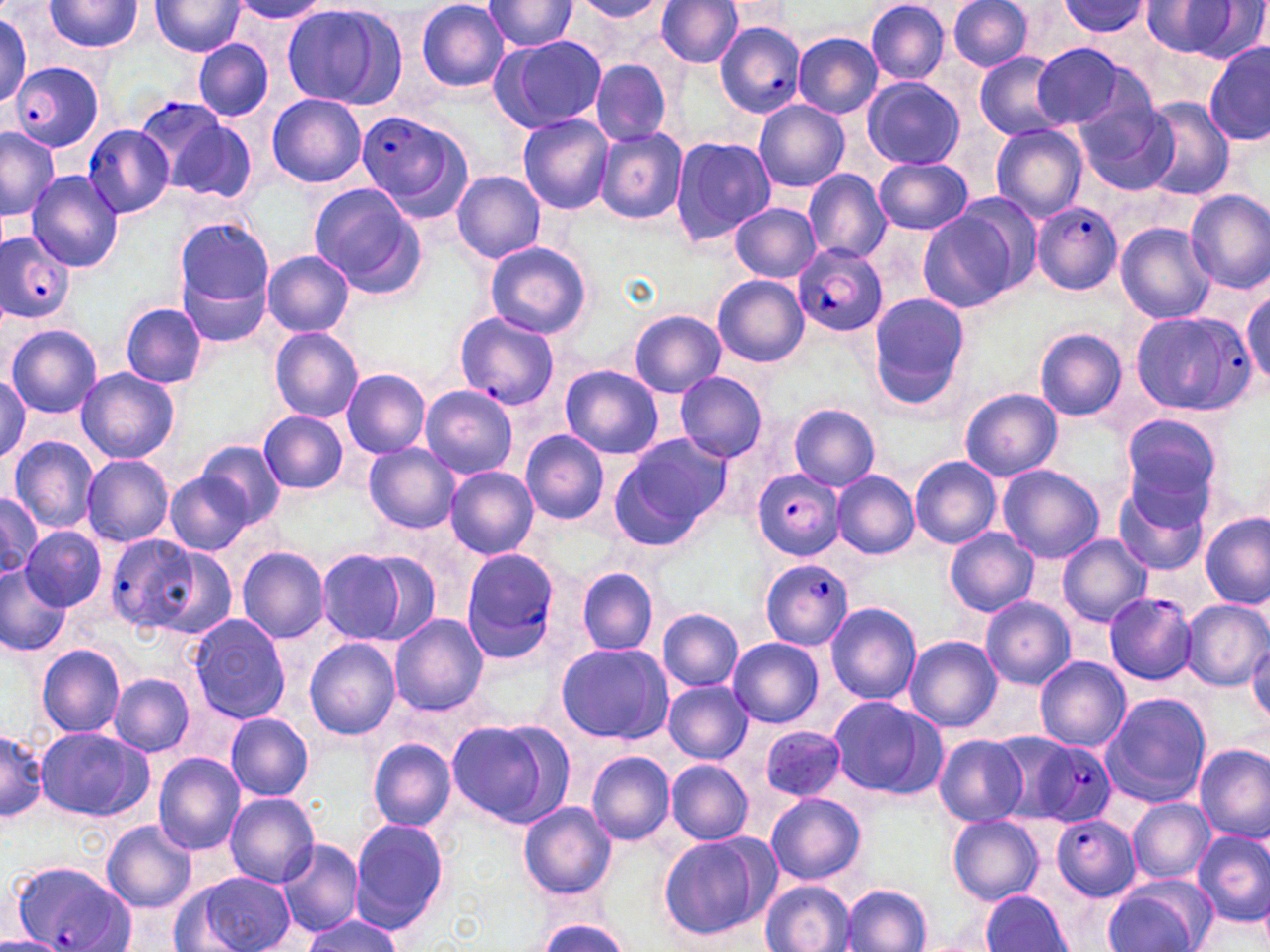
Summary:
  - Coordinate format: approximate bounding boxes as (x1, y1, x2, y2) in pixels
  - Plasmodium falciparum-infected red blood cell locations: (714, 21, 808, 118), (11, 62, 103, 150), (130, 94, 227, 188), (356, 110, 471, 217), (84, 124, 174, 218), (1032, 202, 1123, 295), (2, 232, 75, 322), (793, 244, 888, 337), (1130, 308, 1259, 419), (454, 312, 560, 412), (753, 471, 846, 558), (106, 534, 200, 632), (458, 547, 566, 662), (760, 559, 854, 650), (1104, 592, 1198, 684), (1016, 733, 1118, 829), (1051, 816, 1141, 899), (11, 860, 132, 952)
  - Uninfected red blood cell locations: (45, 0, 144, 52), (484, 0, 578, 53), (719, 0, 794, 29), (865, 0, 949, 83), (946, 0, 1036, 72), (150, 1, 246, 57), (232, 1, 329, 25), (416, 1, 509, 91), (571, 1, 667, 22), (1052, 1, 1155, 40), (658, 2, 745, 69), (280, 3, 401, 110), (1138, 3, 1255, 60), (0, 11, 32, 109), (791, 31, 882, 118), (490, 34, 607, 132), (193, 39, 274, 121), (1030, 42, 1130, 128), (1204, 43, 1268, 144), (974, 51, 1073, 140), (591, 60, 673, 146), (861, 77, 964, 169), (267, 92, 368, 188), (1072, 96, 1179, 197), (1141, 98, 1235, 201), (754, 100, 849, 193), (518, 113, 613, 214), (171, 118, 258, 206), (990, 124, 1086, 223), (594, 128, 688, 225), (0, 129, 59, 220), (670, 133, 776, 246), (871, 157, 973, 234), (26, 171, 123, 273), (452, 171, 546, 262), (802, 171, 890, 262), (309, 184, 424, 297), (1185, 191, 1269, 293), (949, 194, 1042, 295), (728, 203, 822, 282), (917, 209, 1019, 310), (175, 218, 275, 307), (1116, 222, 1218, 325), (166, 227, 330, 331), (484, 242, 593, 340), (261, 251, 355, 337), (177, 263, 274, 348), (713, 275, 810, 367), (1241, 284, 1270, 388), (866, 294, 971, 409), (119, 302, 208, 389), (628, 310, 726, 397), (6, 324, 102, 417), (269, 326, 363, 423), (1034, 327, 1128, 422), (559, 365, 663, 459), (76, 368, 181, 464), (341, 369, 430, 458), (674, 372, 768, 463), (0, 375, 31, 465), (648, 377, 763, 530), (419, 384, 517, 480), (961, 387, 1061, 481), (787, 403, 881, 491), (259, 410, 348, 493), (1120, 413, 1224, 517), (521, 431, 610, 525), (609, 434, 731, 547), (9, 436, 99, 533), (198, 441, 286, 525), (457, 442, 608, 542), (364, 445, 460, 534), (82, 454, 173, 547), (910, 456, 1002, 549), (997, 465, 1105, 564), (445, 466, 539, 560), (832, 471, 919, 560), (165, 472, 254, 556), (1113, 482, 1211, 574), (0, 489, 45, 582), (1200, 513, 1269, 609), (21, 526, 107, 611), (943, 527, 1038, 617), (1057, 534, 1151, 626), (147, 547, 239, 642), (237, 547, 329, 643), (317, 550, 411, 643), (356, 550, 440, 645), (0, 563, 68, 658), (578, 568, 658, 655), (980, 596, 1075, 688), (1177, 599, 1270, 691), (826, 602, 921, 705), (657, 607, 743, 692), (389, 613, 488, 717), (187, 615, 290, 723), (904, 635, 1002, 733), (728, 637, 824, 727), (1246, 637, 1270, 723), (305, 638, 401, 739), (554, 641, 671, 743), (37, 644, 126, 738), (1035, 656, 1131, 752), (110, 673, 195, 755), (664, 680, 752, 763), (1101, 693, 1211, 808), (828, 697, 949, 800), (225, 713, 314, 800), (447, 717, 574, 829), (758, 724, 849, 802), (0, 726, 48, 826), (34, 726, 152, 822), (934, 735, 1027, 826), (367, 738, 456, 831), (1194, 742, 1270, 842), (586, 751, 676, 845), (153, 753, 245, 854), (665, 759, 754, 844), (766, 791, 866, 885), (224, 793, 320, 887), (1128, 797, 1213, 883), (519, 801, 616, 898), (947, 814, 1044, 905), (349, 818, 450, 933), (103, 822, 197, 912), (1193, 829, 1270, 927), (656, 834, 774, 940), (276, 838, 364, 936), (184, 871, 296, 951), (1104, 875, 1216, 952), (759, 880, 854, 952), (842, 884, 931, 952), (980, 889, 1071, 951), (302, 912, 405, 951), (532, 915, 633, 952), (0, 935, 70, 952)
  - Slide-level diagnosis: Plasmodium falciparum
  - Modality: light microscopy
  - Preparation: thin blood smear
  - Stain: May-Grünwald-Giemsa
  - Image size: 1270×952 pixels
  - Magnification: 1000x
  - Field of view: single